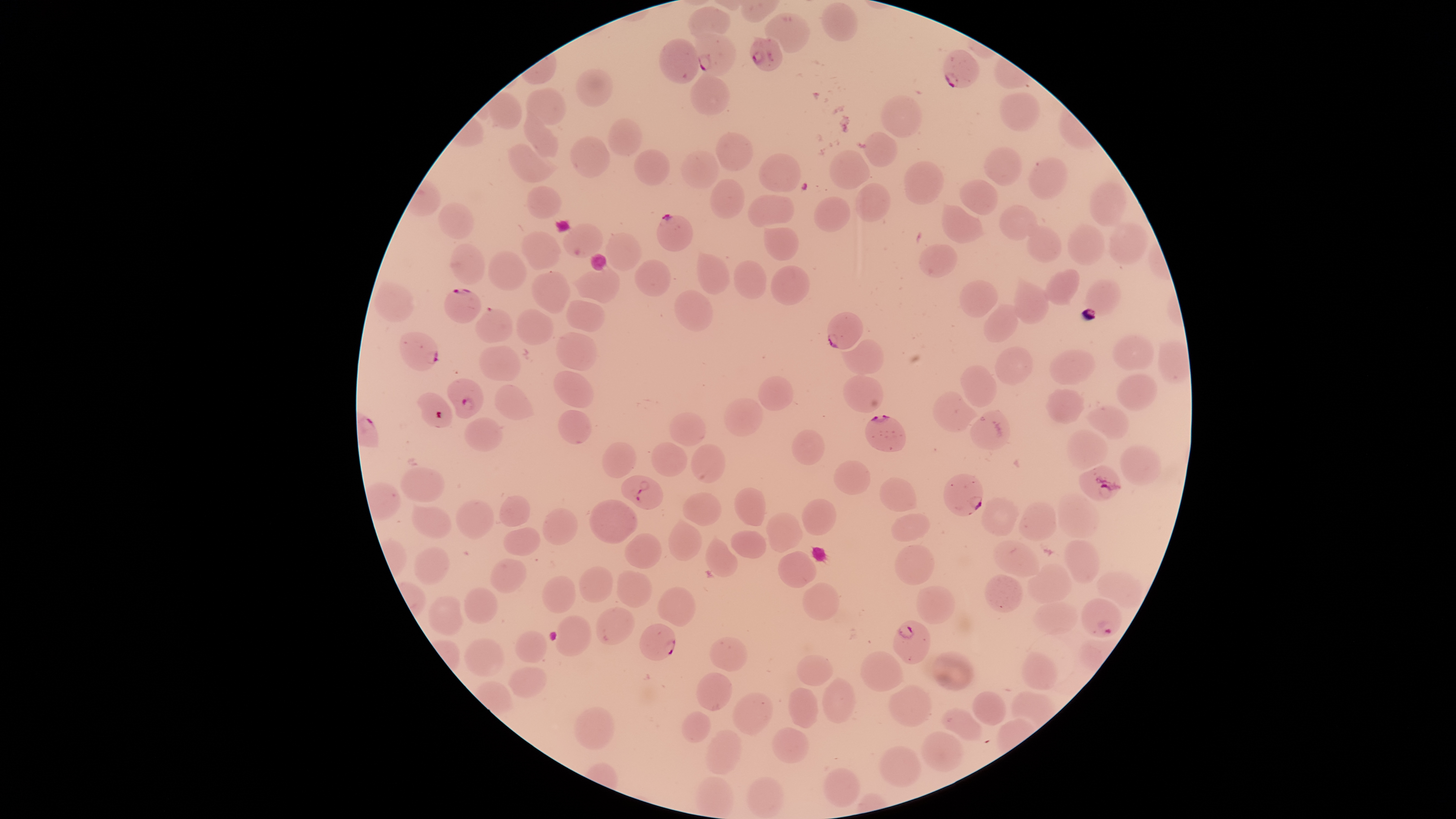 Approximate bounding boxes, in pixels from the top-left corner. Uninfected red blood cells: (left=821, top=2, right=859, bottom=42), (left=687, top=5, right=732, bottom=35), (left=764, top=11, right=810, bottom=53), (left=659, top=37, right=700, bottom=84), (left=576, top=68, right=613, bottom=106), (left=689, top=71, right=731, bottom=115), (left=526, top=86, right=567, bottom=126), (left=999, top=91, right=1040, bottom=132), (left=880, top=95, right=923, bottom=138), (left=523, top=106, right=559, bottom=158), (left=607, top=117, right=643, bottom=157), (left=862, top=130, right=898, bottom=167), (left=715, top=131, right=754, bottom=172), (left=569, top=135, right=611, bottom=179), (left=507, top=143, right=557, bottom=183), (left=983, top=145, right=1023, bottom=186), (left=633, top=148, right=671, bottom=185), (left=679, top=149, right=720, bottom=189), (left=828, top=149, right=870, bottom=190), (left=758, top=152, right=802, bottom=193), (left=1028, top=156, right=1067, bottom=200), (left=903, top=160, right=945, bottom=204), (left=710, top=178, right=745, bottom=220), (left=959, top=179, right=999, bottom=215), (left=1088, top=181, right=1128, bottom=227), (left=855, top=182, right=891, bottom=222), (left=525, top=185, right=563, bottom=219), (left=747, top=194, right=795, bottom=228), (left=813, top=196, right=851, bottom=233), (left=437, top=200, right=474, bottom=240), (left=941, top=203, right=986, bottom=243), (left=999, top=204, right=1039, bottom=241), (left=1024, top=221, right=1062, bottom=263), (left=1108, top=221, right=1150, bottom=265), (left=562, top=222, right=604, bottom=258), (left=1066, top=223, right=1106, bottom=265), (left=762, top=225, right=800, bottom=261), (left=520, top=230, right=562, bottom=269), (left=602, top=232, right=642, bottom=271), (left=449, top=243, right=485, bottom=285), (left=918, top=244, right=959, bottom=277), (left=487, top=250, right=527, bottom=291), (left=696, top=252, right=731, bottom=295), (left=634, top=259, right=671, bottom=297), (left=733, top=260, right=767, bottom=299), (left=770, top=264, right=811, bottom=305), (left=569, top=266, right=621, bottom=304), (left=1043, top=268, right=1080, bottom=306), (left=530, top=271, right=572, bottom=313), (left=1013, top=274, right=1049, bottom=325), (left=1084, top=278, right=1122, bottom=316), (left=959, top=279, right=999, bottom=317), (left=373, top=281, right=415, bottom=323), (left=674, top=289, right=713, bottom=332), (left=565, top=299, right=606, bottom=332), (left=983, top=303, right=1020, bottom=342), (left=516, top=308, right=554, bottom=345), (left=555, top=331, right=599, bottom=371), (left=1112, top=333, right=1155, bottom=371), (left=841, top=338, right=884, bottom=375), (left=478, top=345, right=521, bottom=381), (left=994, top=345, right=1034, bottom=385), (left=1049, top=349, right=1097, bottom=385), (left=960, top=364, right=997, bottom=408), (left=553, top=370, right=595, bottom=408), (left=843, top=374, right=885, bottom=414), (left=1116, top=374, right=1158, bottom=411), (left=758, top=375, right=794, bottom=411), (left=494, top=383, right=535, bottom=420), (left=1046, top=388, right=1085, bottom=424), (left=932, top=391, right=981, bottom=432), (left=722, top=396, right=763, bottom=436), (left=1085, top=405, right=1131, bottom=439), (left=557, top=409, right=593, bottom=444), (left=969, top=410, right=1012, bottom=451), (left=668, top=412, right=707, bottom=446), (left=463, top=417, right=504, bottom=452), (left=791, top=428, right=826, bottom=466), (left=1066, top=429, right=1109, bottom=471), (left=602, top=441, right=637, bottom=479), (left=650, top=441, right=689, bottom=477), (left=690, top=444, right=726, bottom=483), (left=1119, top=445, right=1163, bottom=487), (left=832, top=460, right=871, bottom=496), (left=400, top=467, right=446, bottom=501), (left=879, top=477, right=919, bottom=511), (left=734, top=486, right=766, bottom=526), (left=682, top=491, right=722, bottom=526), (left=499, top=494, right=531, bottom=527), (left=1058, top=494, right=1100, bottom=539), (left=980, top=496, right=1020, bottom=537), (left=589, top=498, right=638, bottom=544), (left=801, top=498, right=837, bottom=535), (left=455, top=499, right=494, bottom=539), (left=1018, top=501, right=1058, bottom=541), (left=411, top=504, right=451, bottom=539), (left=542, top=507, right=578, bottom=545), (left=765, top=512, right=804, bottom=553), (left=891, top=512, right=931, bottom=542), (left=668, top=518, right=703, bottom=562), (left=502, top=526, right=541, bottom=556), (left=730, top=529, right=767, bottom=559), (left=623, top=532, right=663, bottom=569), (left=705, top=536, right=739, bottom=577), (left=992, top=539, right=1040, bottom=577), (left=1064, top=539, right=1101, bottom=586), (left=894, top=543, right=935, bottom=585), (left=413, top=546, right=451, bottom=585), (left=777, top=550, right=817, bottom=588), (left=489, top=558, right=527, bottom=593), (left=1026, top=562, right=1073, bottom=604), (left=578, top=565, right=613, bottom=602), (left=616, top=570, right=652, bottom=608), (left=1096, top=571, right=1144, bottom=609), (left=984, top=573, right=1024, bottom=613), (left=541, top=574, right=576, bottom=613), (left=801, top=582, right=840, bottom=621), (left=915, top=585, right=956, bottom=624), (left=464, top=586, right=499, bottom=624), (left=657, top=586, right=696, bottom=627), (left=427, top=594, right=465, bottom=636), (left=1032, top=601, right=1080, bottom=636), (left=595, top=606, right=636, bottom=645), (left=555, top=615, right=592, bottom=656), (left=514, top=630, right=547, bottom=663), (left=709, top=636, right=748, bottom=673), (left=463, top=637, right=505, bottom=678), (left=860, top=650, right=903, bottom=692), (left=931, top=650, right=975, bottom=692), (left=1020, top=651, right=1059, bottom=690), (left=795, top=654, right=834, bottom=686), (left=506, top=665, right=548, bottom=698), (left=695, top=672, right=733, bottom=711), (left=821, top=676, right=856, bottom=723), (left=888, top=684, right=933, bottom=727), (left=787, top=686, right=819, bottom=729), (left=971, top=691, right=1007, bottom=726), (left=1010, top=691, right=1057, bottom=729), (left=731, top=692, right=773, bottom=735), (left=573, top=706, right=615, bottom=751), (left=939, top=707, right=983, bottom=741), (left=680, top=711, right=711, bottom=743), (left=770, top=727, right=810, bottom=763), (left=704, top=729, right=743, bottom=774), (left=920, top=731, right=964, bottom=772), (left=878, top=745, right=922, bottom=788), (left=823, top=767, right=861, bottom=808), (left=694, top=775, right=735, bottom=818), (left=747, top=776, right=784, bottom=818). Parasitized red blood cells: (left=694, top=31, right=737, bottom=76), (left=748, top=36, right=783, bottom=71), (left=942, top=49, right=980, bottom=89), (left=656, top=213, right=694, bottom=252), (left=444, top=288, right=483, bottom=324), (left=475, top=307, right=513, bottom=344), (left=827, top=311, right=864, bottom=350), (left=398, top=331, right=439, bottom=372), (left=446, top=377, right=485, bottom=419), (left=417, top=392, right=454, bottom=428), (left=865, top=414, right=907, bottom=452), (left=1078, top=465, right=1121, bottom=501), (left=942, top=473, right=983, bottom=516), (left=620, top=475, right=664, bottom=510), (left=1081, top=598, right=1123, bottom=638), (left=892, top=619, right=930, bottom=665), (left=639, top=623, right=676, bottom=661). Giemsa-stained preparation. Presence: malaria parasites seen. Image is 1456×819 pixels. Smartphone photograph through the microscope eyepiece. Species: Plasmodium falciparum. The visible region is circular. One field of view of the specimen. Thin blood smear.